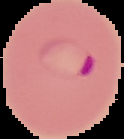

preparation = thin blood film
image size = 124×139 pixels
result = Plasmodium parasites detected
image type = segmented cell region on a black background